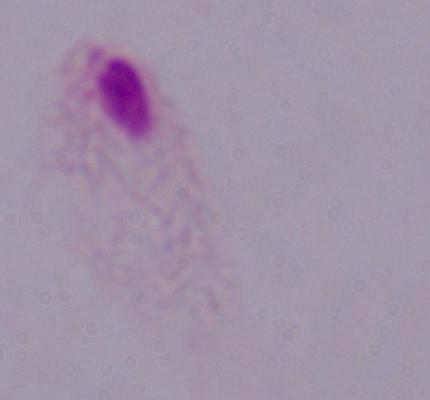
Summary:
  - Identification: trichomonad
  - Magnification: 1000x
  - Modality: micrograph